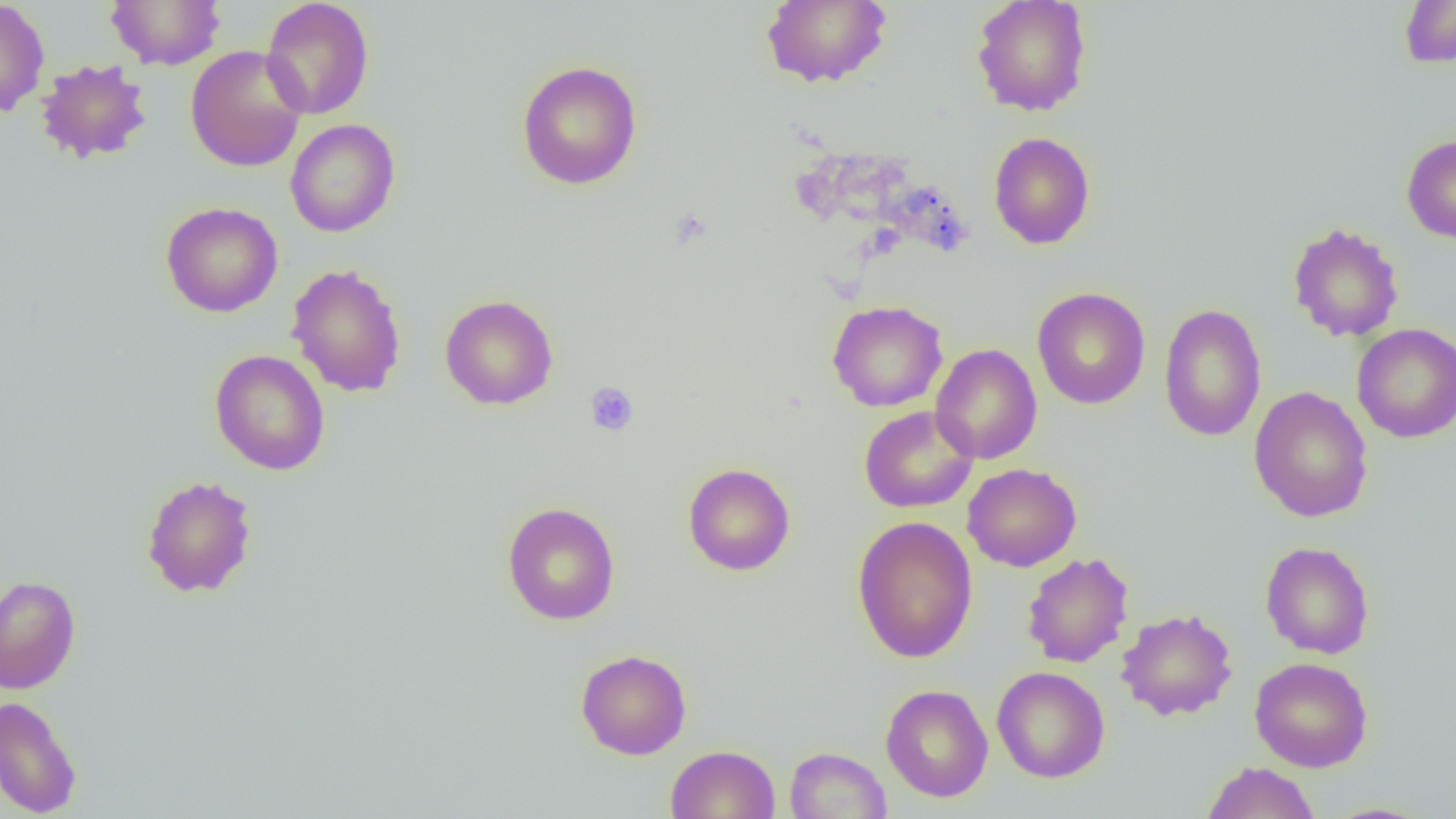
slide-level diagnosis = negative for blood parasites
platelet locations = approximate bounding boxes as (x1,y1)-(x2,y2) corner pairs in pixels: (585,382)-(638,436)
uninfected red blood cell locations = approximate bounding boxes as (x1,y1)-(x2,y2) corner pairs in pixels: (0,0)-(50,118), (106,0)-(226,70), (260,0)-(374,120), (761,0)-(892,88), (971,0)-(1092,116), (1399,0)-(1456,68), (185,45)-(307,172), (35,58)-(153,164), (516,60)-(643,190), (285,119)-(400,237), (988,132)-(1095,249), (1401,134)-(1456,243), (160,201)-(283,317), (1287,222)-(1404,342), (286,263)-(407,398), (1032,287)-(1150,409), (440,294)-(559,411), (827,300)-(948,412), (1158,302)-(1266,442), (1352,323)-(1456,443), (930,343)-(1042,464), (209,349)-(330,475), (1248,387)-(1374,522), (859,405)-(978,513), (682,462)-(796,576), (963,464)-(1081,572), (141,475)-(257,598), (502,502)-(620,625), (851,515)-(978,663), (1260,541)-(1375,659), (1021,552)-(1134,668), (0,575)-(81,694), (1117,608)-(1237,721), (575,649)-(692,760), (1249,656)-(1373,772), (992,666)-(1110,783), (880,684)-(993,802), (0,695)-(82,818), (665,744)-(780,819), (785,746)-(892,819), (1201,761)-(1321,819), (1321,802)-(1438,819)
magnification = 1000x
field of view = one of a larger specimen
preparation = thin blood smear
modality = optical microscopy
image size = 1456×819 pixels